Point out each Plasmodium parasite.
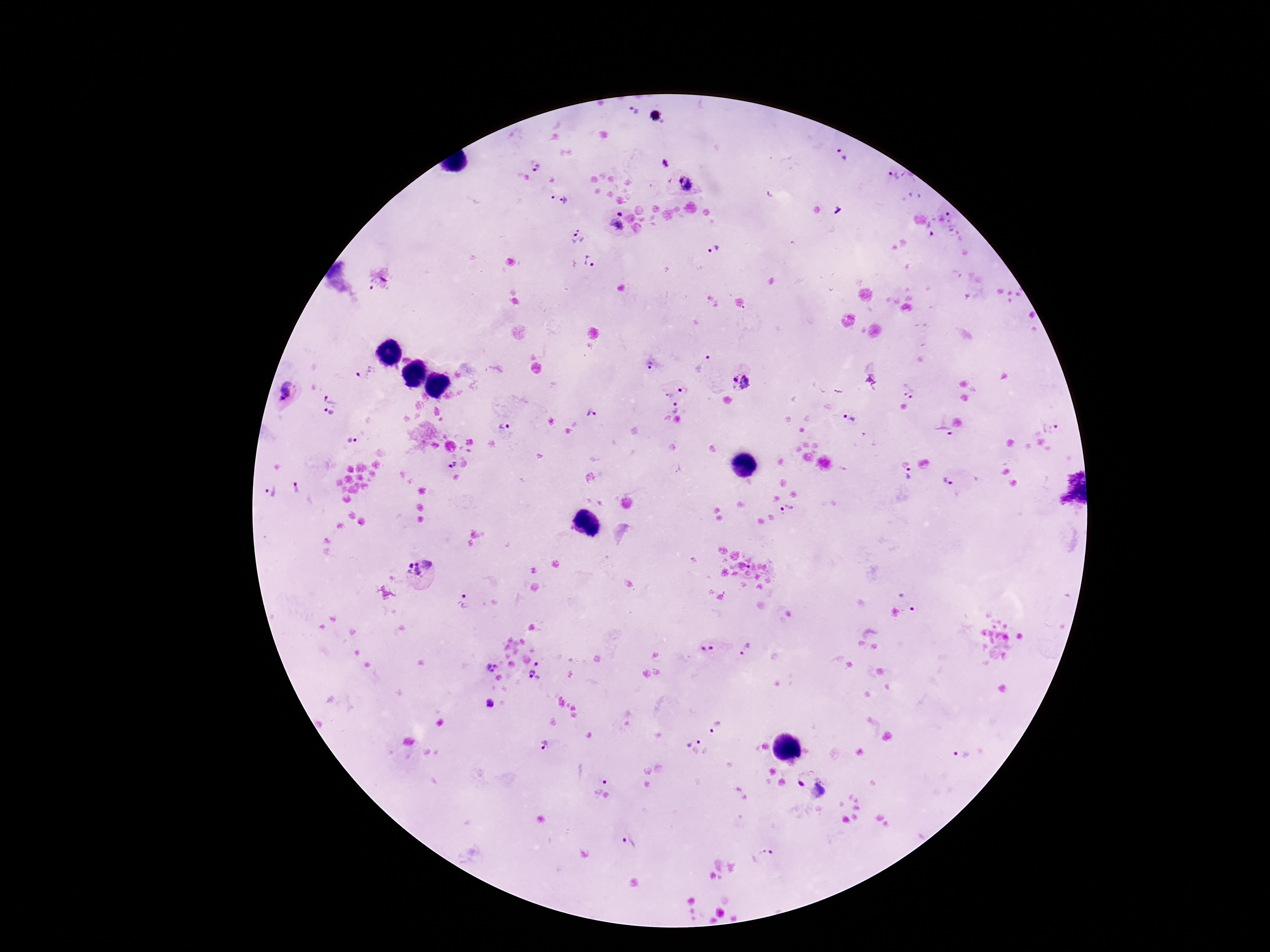

Approximate centers as (x, y) in pixels.
Plasmodium parasites: (634, 110), (842, 156), (665, 162), (536, 167), (892, 174), (686, 183), (558, 200), (951, 217), (616, 221), (930, 229), (577, 236), (715, 248), (589, 260), (649, 364), (704, 364), (364, 371), (743, 382), (908, 388), (683, 391), (286, 392), (668, 395), (331, 397), (677, 407), (329, 413), (591, 414), (849, 419), (503, 428), (1050, 428), (940, 429), (351, 442), (452, 465), (910, 473), (948, 480), (296, 487), (269, 491), (787, 510), (419, 569), (908, 598), (462, 601), (708, 649), (745, 649), (491, 667), (535, 675), (489, 704), (716, 727), (694, 740), (546, 745), (960, 753), (801, 783), (596, 784), (819, 788), (630, 841), (763, 858).

capture = smartphone camera through the microscope eyepiece
stain = Giemsa
magnification = 100x
field of view = single
preparation = thick peripheral-blood smear
patient malaria status = positive
image size = 1270×952 pixels